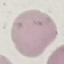
Summary:
  - Result: no malaria parasites seen
  - Preparation: thin blood film
  - Capture: smartphone camera at the microscope eyepiece
  - Image type: cell patch, automatically extracted from a larger field of view and resized to 64 × 64 pixels
  - Stain: Giemsa